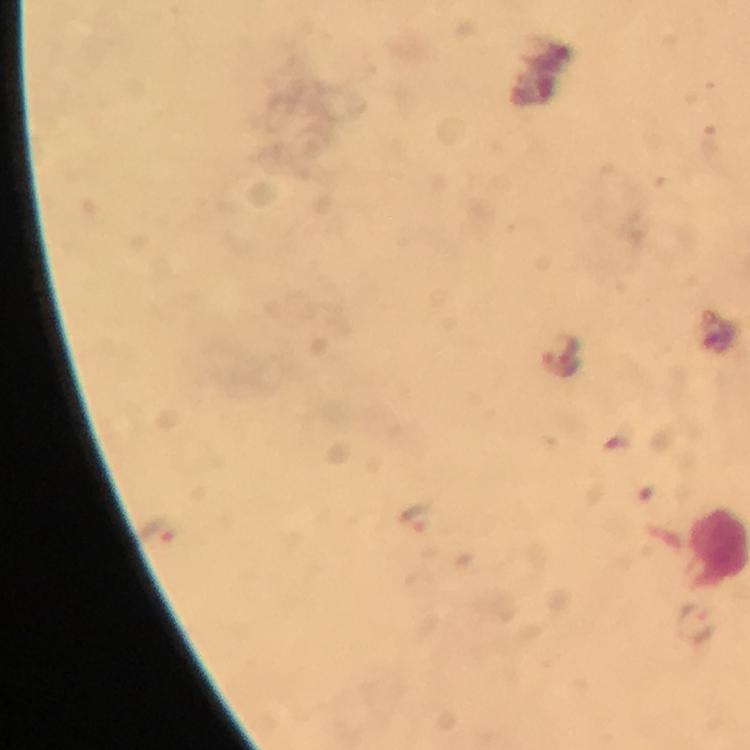 Approximate centers as {x, y} in pixels. Malaria parasite locations: {569, 346}, {563, 363}, {414, 519}, {155, 529}, {695, 623}. 100x magnification. From a malaria diagnostic workup. Thick blood film. Photographed with a smartphone mounted on the microscope. Image is 750×750 pixels. Giemsa stain. Cropped region of a single field of view. Immersion oil applied.